Outline each Plasmodium falciparum-infected red blood cell.
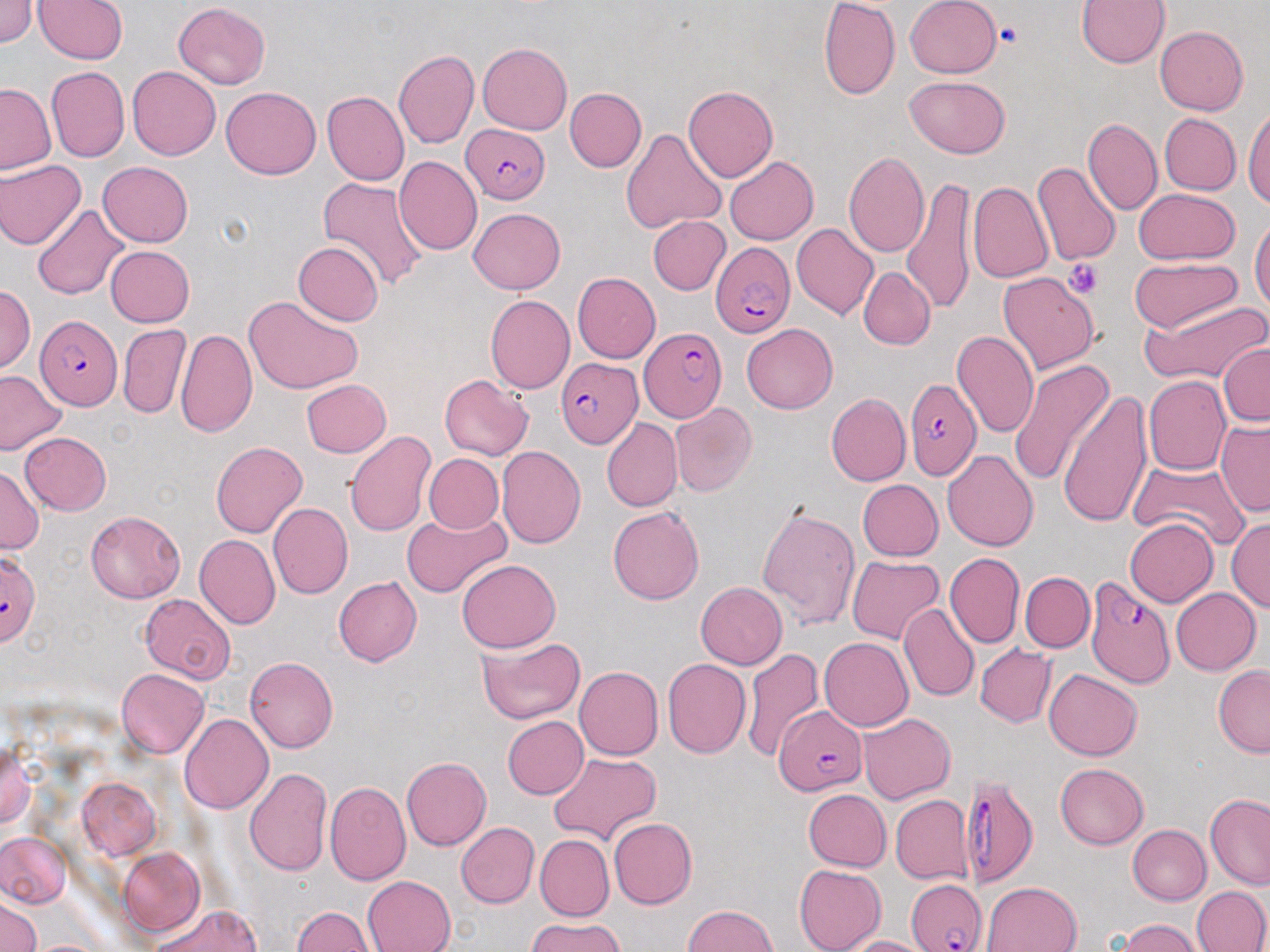

Approximate bounding boxes as (x1, y1, x2, y2) in pixels.
Plasmodium falciparum-infected red blood cells (subset): (458, 124, 548, 202), (710, 241, 793, 337), (35, 316, 121, 408), (639, 327, 727, 422), (555, 358, 640, 448), (904, 374, 983, 478), (1085, 574, 1177, 690), (774, 704, 866, 795), (958, 774, 1039, 886).

{
  "slide_level_diagnosis": "Plasmodium falciparum",
  "uninfected_red_blood_cell_locations_subset": "approximate bounding boxes as (x1, y1, x2, y2) in pixels: (0, 0, 37, 49), (35, 0, 128, 64), (905, 0, 1003, 78), (1078, 0, 1169, 69), (821, 1, 899, 99), (171, 2, 272, 88), (1154, 25, 1250, 114), (478, 42, 575, 135), (394, 49, 480, 148), (127, 67, 220, 159), (44, 68, 128, 164), (903, 76, 1012, 158), (1, 82, 57, 176), (685, 83, 781, 182), (221, 87, 321, 180), (565, 87, 646, 172), (323, 90, 410, 184), (1243, 108, 1270, 211), (1157, 113, 1240, 197), (1083, 117, 1161, 218), (620, 126, 726, 235), (844, 151, 931, 256), (393, 156, 481, 255), (723, 156, 817, 245), (0, 159, 83, 250), (98, 162, 193, 245), (1033, 163, 1120, 265), (315, 177, 427, 296), (903, 179, 978, 312), (967, 179, 1054, 286), (1133, 189, 1239, 264), (33, 203, 132, 303), (467, 207, 564, 293), (648, 215, 731, 296), (1251, 217, 1269, 319), (790, 221, 878, 319), (294, 240, 384, 327), (105, 245, 195, 327), (1127, 258, 1242, 335), (859, 266, 935, 350), (998, 268, 1099, 374), (573, 273, 661, 363), (1, 283, 35, 377), (243, 296, 364, 393), (485, 296, 574, 395), (1143, 297, 1270, 388), (118, 323, 191, 419), (740, 323, 837, 414), (175, 326, 256, 437), (953, 330, 1039, 437), (1220, 343, 1270, 430), (1008, 358, 1112, 485), (0, 368, 68, 457), (439, 375, 533, 459), (1142, 376, 1230, 477), (301, 379, 390, 458), (1058, 391, 1152, 527), (824, 393, 909, 487), (670, 404, 755, 496), (601, 420, 681, 513), (1216, 422, 1270, 517), (344, 429, 437, 540), (20, 432, 111, 516), (211, 441, 308, 539), (497, 446, 585, 548), (943, 449, 1038, 553), (425, 455, 503, 534), (1127, 455, 1250, 550), (0, 467, 44, 555), (855, 480, 942, 561), (757, 502, 861, 632), (268, 503, 352, 599), (608, 506, 705, 604), (84, 509, 185, 601), (401, 512, 510, 597), (1123, 518, 1217, 607), (1228, 520, 1269, 617), (195, 535, 281, 628), (0, 546, 43, 649), (946, 551, 1024, 649), (847, 556, 945, 646), (458, 558, 560, 651), (1020, 571, 1094, 654), (334, 577, 422, 666), (695, 580, 788, 669), (1169, 587, 1259, 676), (139, 595, 236, 683), (900, 603, 978, 702), (819, 636, 913, 730), (476, 638, 585, 725), (745, 644, 824, 760), (976, 644, 1056, 729), (246, 655, 339, 751), (661, 657, 751, 760), (1212, 665, 1270, 756), (575, 667, 663, 759), (117, 668, 209, 758), (1043, 670, 1142, 760), (859, 711, 954, 804), (180, 712, 273, 811), (500, 715, 588, 800), (0, 737, 38, 839), (548, 751, 662, 843), (402, 755, 492, 850), (1054, 763, 1148, 849), (244, 767, 332, 877), (77, 779, 163, 860), (326, 780, 410, 884), (803, 789, 890, 871), (890, 794, 972, 885), (1204, 795, 1270, 887), (610, 816, 697, 908), (456, 822, 539, 908), (1128, 824, 1210, 904), (0, 831, 74, 911), (536, 836, 613, 917), (117, 849, 207, 939), (793, 864, 886, 952), (362, 875, 453, 952), (982, 881, 1084, 952), (1192, 886, 1268, 952), (0, 896, 42, 952), (145, 903, 264, 952), (681, 903, 784, 952), (289, 907, 375, 952), (523, 918, 627, 952), (1118, 919, 1199, 952), (843, 934, 927, 952)",
  "stain": "May-Grünwald-Giemsa",
  "platelet_locations": "approximate bounding boxes as (x1, y1, x2, y2) in pixels: (992, 22, 1023, 46), (1065, 257, 1105, 299)",
  "field_of_view": "one of a larger specimen",
  "magnification": "1000x",
  "image_size": "1270×952 pixels",
  "modality": "light microscopy",
  "preparation": "thin blood film"
}